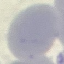 Malaria status: uninfected. Acquired by smartphone through the microscope eyepiece. Giemsa-stained preparation. Automatically extracted cell patch, resized to 64 × 64 pixels. Thin blood film.